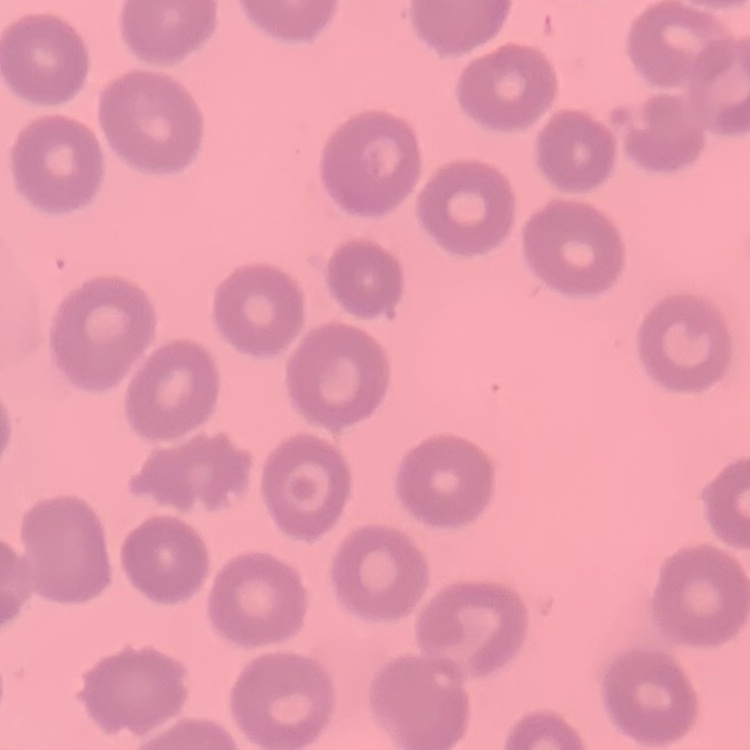

The erythrocytes show no rouleaux formation. Thin peripheral smear. Field's or Giemsa stain. One tile cut from a larger photomicrograph.